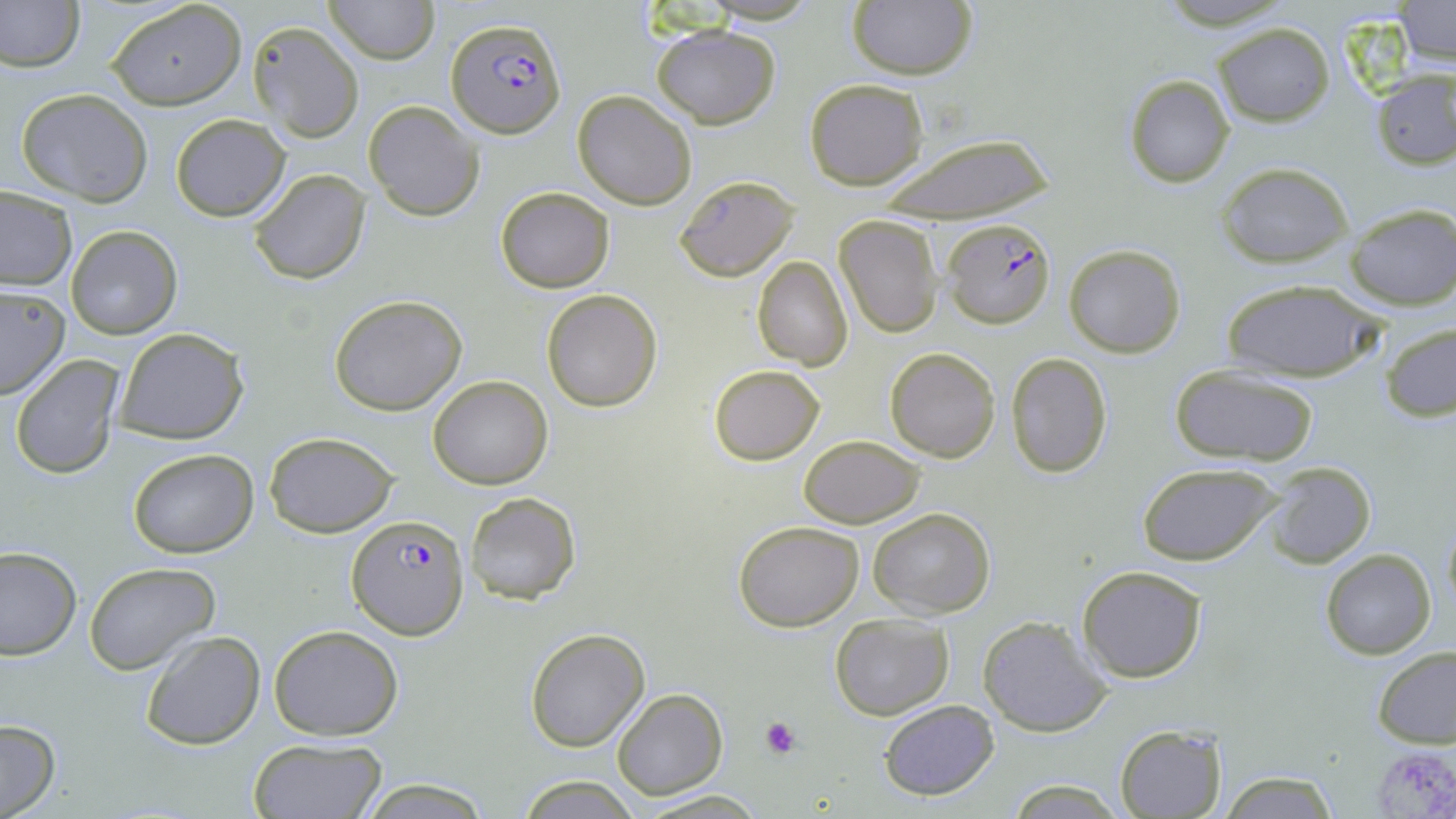 Approximate bounding boxes as [x1, y1, x2, y2] in pixels. Uninfected red blood cell locations: [0, 0, 84, 72], [324, 0, 437, 64], [847, 1, 977, 80], [108, 2, 245, 109], [1391, 2, 1454, 67], [247, 20, 364, 143], [1214, 23, 1333, 127], [650, 24, 779, 128], [1370, 69, 1456, 170], [1123, 73, 1235, 188], [804, 78, 928, 188], [15, 88, 153, 206], [573, 92, 696, 210], [364, 100, 483, 221], [169, 112, 289, 222], [876, 134, 1056, 223], [1216, 162, 1354, 267], [249, 169, 371, 284], [674, 174, 800, 281], [494, 186, 615, 293], [0, 187, 76, 290], [1344, 203, 1455, 310], [833, 214, 943, 337], [66, 225, 181, 339], [1063, 244, 1186, 357], [753, 256, 854, 371], [1219, 278, 1385, 383], [0, 287, 71, 400], [541, 289, 663, 412], [329, 294, 467, 416], [1381, 323, 1456, 423], [113, 327, 249, 444], [884, 348, 1000, 463], [1005, 352, 1114, 478], [11, 355, 124, 479], [708, 363, 825, 465], [1169, 366, 1319, 465], [428, 375, 552, 489], [264, 430, 399, 537], [798, 435, 924, 527], [128, 449, 258, 557], [1136, 462, 1282, 567], [1263, 462, 1376, 568], [463, 491, 580, 604], [867, 506, 996, 619], [1441, 516, 1456, 619], [733, 520, 864, 632], [0, 547, 79, 660], [1320, 548, 1436, 660], [83, 561, 220, 675], [1077, 565, 1206, 682], [830, 613, 954, 719], [978, 617, 1109, 738], [267, 624, 404, 739], [525, 628, 649, 752], [140, 631, 265, 750], [1373, 646, 1456, 748], [611, 688, 727, 799], [879, 698, 999, 801], [0, 720, 60, 817], [1115, 724, 1227, 817], [247, 738, 387, 819], [1217, 769, 1344, 819], [516, 774, 642, 818], [360, 779, 490, 816], [1003, 781, 1125, 814], [630, 789, 771, 819]. Platelet locations: [760, 715, 800, 758], [1375, 749, 1456, 818]. Plasmodium falciparum-infected red blood cell locations: [448, 16, 566, 137], [944, 221, 1056, 331], [347, 514, 470, 639]. Slide-level diagnosis: Plasmodium falciparum. Captured at 1000x magnification. Image is 1456×819 pixels. May-Grünwald-Giemsa stain. Thin blood film. Single field of view. Light microscopy.